Name the parasite shown.
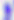
Toxoplasma gondii.

Micrograph. 400x magnification.